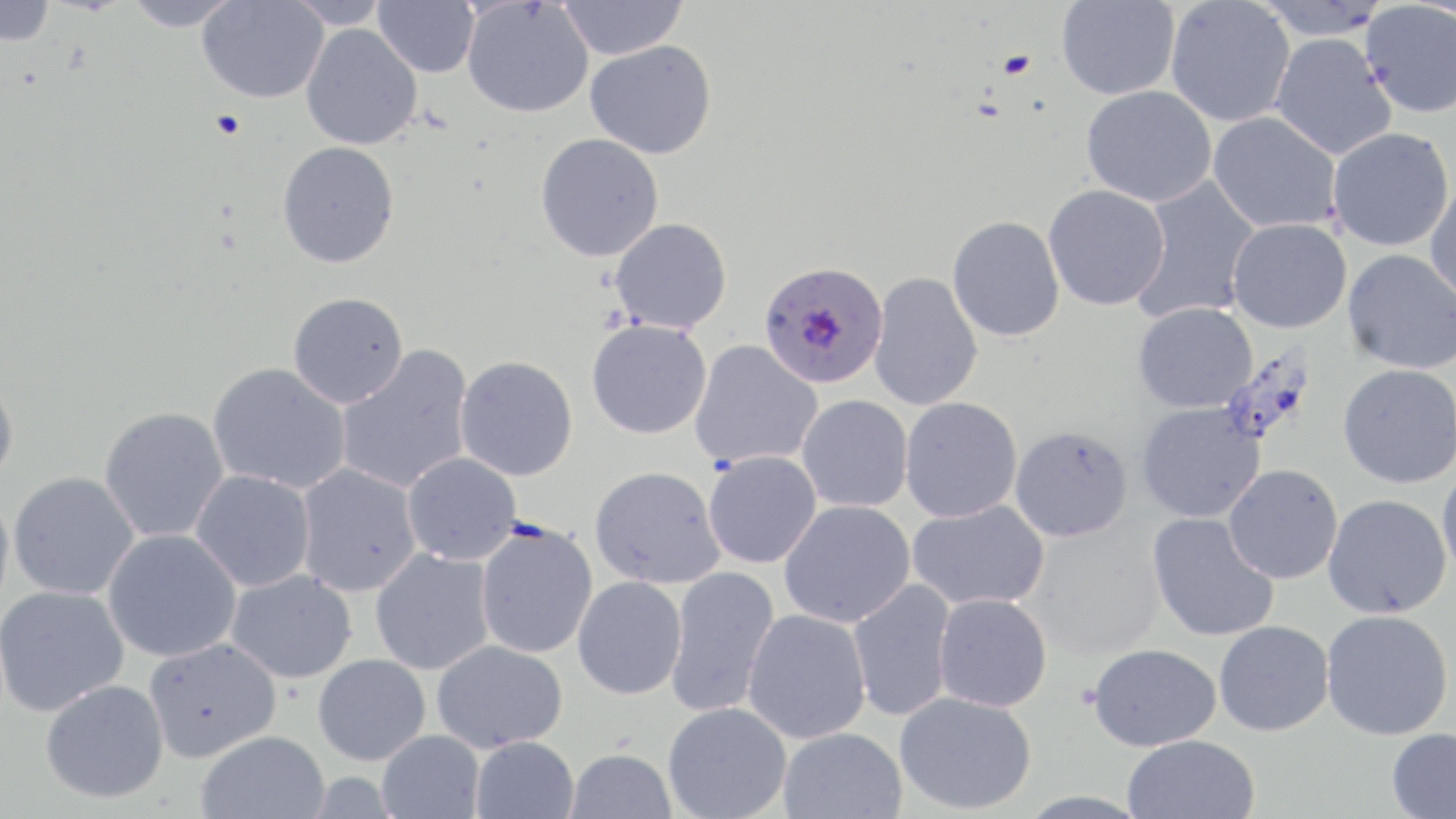
Approximate bounding boxes as (x1, y1, x2, y2) in pixels. Uninfected red blood cell locations: (0, 0, 55, 46), (123, 0, 242, 31), (197, 0, 328, 103), (286, 0, 392, 29), (373, 0, 479, 78), (558, 0, 687, 60), (461, 1, 593, 118), (1056, 1, 1181, 100), (1166, 1, 1295, 127), (1251, 1, 1390, 40), (1360, 2, 1456, 119), (300, 23, 423, 150), (1270, 33, 1397, 160), (585, 40, 717, 159), (1081, 85, 1218, 207), (1208, 112, 1342, 233), (1327, 128, 1454, 252), (535, 133, 664, 262), (277, 141, 399, 268), (1130, 176, 1261, 324), (1425, 176, 1456, 308), (1043, 185, 1170, 311), (947, 215, 1065, 342), (610, 218, 732, 333), (1227, 218, 1352, 333), (1342, 249, 1456, 374), (868, 273, 983, 411), (287, 292, 408, 408), (1133, 302, 1258, 413), (586, 319, 712, 440), (689, 339, 823, 469), (335, 345, 475, 495), (455, 356, 578, 481), (208, 362, 351, 495), (1337, 363, 1456, 488), (0, 378, 18, 486), (797, 395, 913, 512), (900, 396, 1022, 522), (1136, 403, 1266, 523), (99, 406, 230, 544), (1010, 425, 1133, 542), (703, 450, 822, 569), (402, 452, 521, 565), (295, 464, 421, 597), (589, 465, 725, 589), (1223, 465, 1343, 584), (1437, 465, 1456, 581), (190, 470, 316, 592), (8, 471, 139, 600), (0, 493, 14, 618), (1323, 494, 1452, 620), (779, 500, 916, 628), (907, 500, 1050, 611), (1146, 513, 1279, 642), (475, 521, 598, 659), (102, 529, 241, 663), (370, 548, 495, 675), (666, 566, 780, 717), (226, 570, 356, 683), (573, 576, 687, 700), (848, 579, 957, 723), (0, 585, 128, 716), (934, 593, 1053, 712), (743, 609, 872, 744), (1320, 610, 1453, 740), (1213, 620, 1334, 736), (143, 638, 281, 762), (432, 640, 568, 752), (1087, 643, 1221, 751), (313, 654, 431, 766), (40, 680, 169, 804), (894, 691, 1037, 814), (663, 702, 792, 819), (778, 727, 906, 819), (1386, 727, 1456, 819), (196, 730, 329, 819), (377, 730, 485, 818), (1122, 735, 1261, 819), (470, 736, 579, 819), (565, 748, 678, 819). Plasmodium falciparum-infected red blood cell locations: (759, 260, 889, 389). Platelet locations: (210, 110, 246, 139). Slide-level diagnosis: Plasmodium falciparum. 1000x magnification. Image is 1456×819 pixels. Light microscopy. Thin blood film. May-Grünwald-Giemsa stain. Single field of view.